Report the malaria status of this cell.
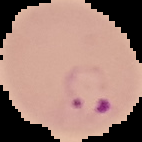

It is parasitized.

Segmented cell region on a black background. Image is 142×142 pixels. From a thin blood film.